Report the malaria status of this cell.
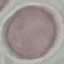

Uninfected.

Photographed with a smartphone camera at the microscope eyepiece. Giemsa stain. Thin smear of blood. Automatically extracted cell patch, resized to 64 × 64 pixels.